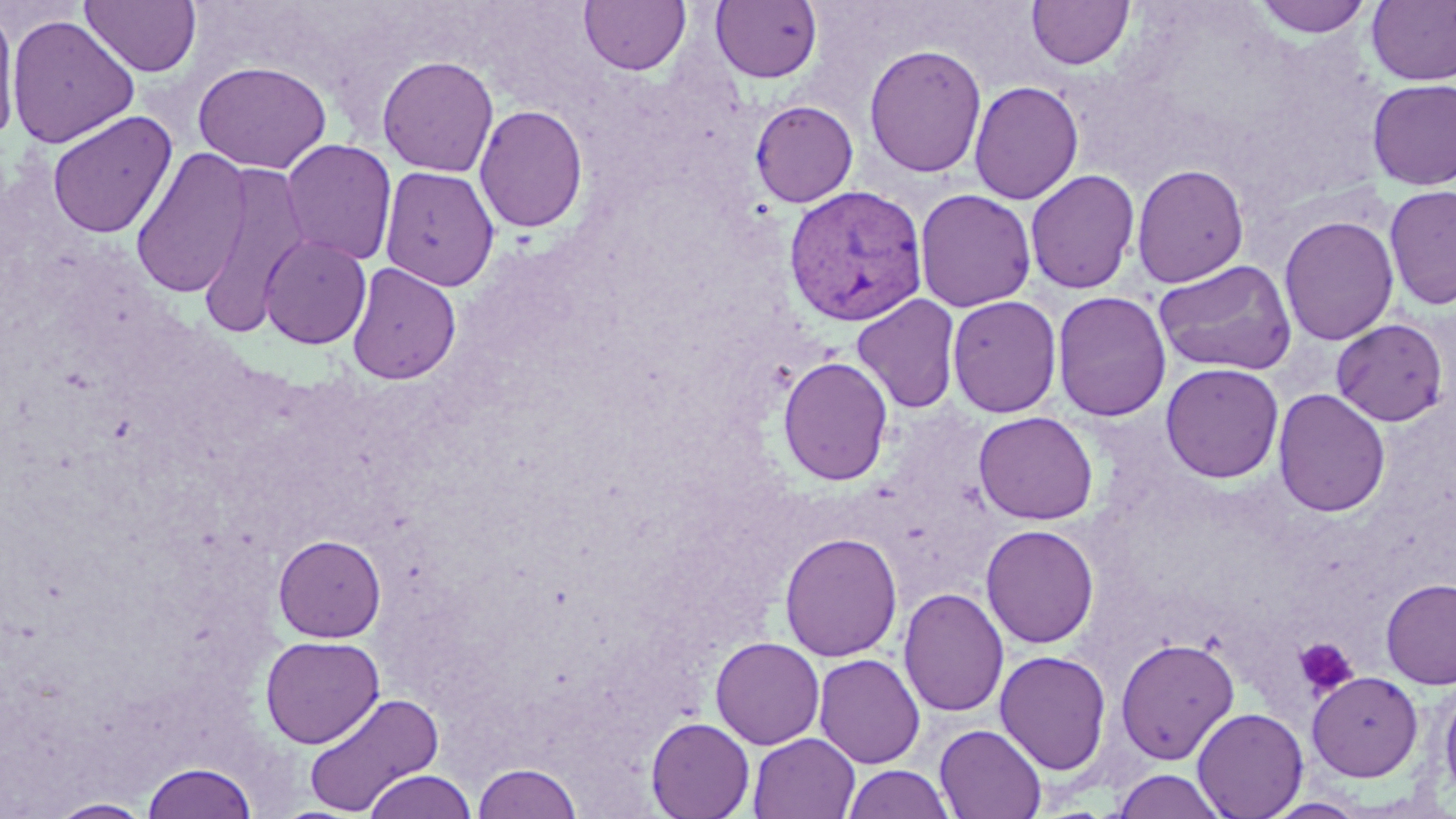
Summary:
  - Coordinate format: approximate bounding boxes as (x1, y1, x2, y2) in pixels
  - Plasmodium vivax-infected red blood cell locations: (784, 184, 929, 327)
  - Uninfected red blood cell locations: (79, 0, 202, 78), (579, 0, 691, 75), (1025, 0, 1134, 71), (1251, 0, 1375, 39), (1366, 0, 1456, 86), (709, 1, 823, 84), (0, 5, 21, 144), (5, 13, 140, 149), (864, 43, 987, 179), (377, 56, 499, 177), (193, 60, 331, 174), (1366, 78, 1456, 191), (968, 80, 1084, 205), (749, 100, 859, 207), (474, 104, 588, 234), (46, 111, 177, 239), (280, 139, 398, 266), (130, 147, 251, 299), (196, 161, 312, 336), (1131, 163, 1249, 288), (380, 166, 501, 290), (1024, 169, 1140, 294), (1383, 184, 1456, 310), (914, 188, 1037, 312), (1279, 215, 1399, 346), (259, 234, 372, 349), (1153, 259, 1297, 377), (346, 262, 461, 384), (1051, 290, 1172, 422), (852, 293, 962, 414), (946, 295, 1062, 418), (1331, 318, 1450, 427), (777, 356, 893, 486), (1160, 362, 1284, 483), (1272, 387, 1390, 517), (973, 411, 1098, 525), (981, 524, 1100, 649), (779, 532, 902, 661), (273, 533, 387, 642), (1380, 578, 1456, 689), (898, 587, 1009, 717), (260, 635, 384, 748), (710, 636, 825, 749), (1115, 636, 1239, 764), (994, 650, 1112, 775), (813, 653, 925, 768), (1307, 671, 1423, 781), (1438, 679, 1456, 806), (302, 690, 445, 816), (1192, 707, 1308, 819), (646, 717, 755, 819), (934, 724, 1047, 819), (748, 733, 860, 819), (141, 760, 259, 819), (473, 762, 584, 819), (841, 764, 956, 819), (362, 769, 478, 819), (1111, 769, 1229, 819), (1262, 797, 1369, 818), (46, 798, 155, 818)
  - Platelet locations: (1294, 637, 1358, 697)
  - Slide-level diagnosis: Plasmodium vivax
  - Magnification: 1000x
  - Stain: May-Grünwald-Giemsa
  - Image size: 1456×819 pixels
  - Field of view: one of a larger specimen
  - Preparation: thin blood film
  - Modality: light microscopy